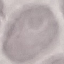
Summary:
  - Result: no malaria parasites detected
  - Capture: smartphone camera at the microscope eyepiece
  - Stain: Giemsa
  - Preparation: thin blood smear
  - Image type: cell patch, automatically extracted from a larger field of view and resized to 64 × 64 pixels